Name the blood parasite species.
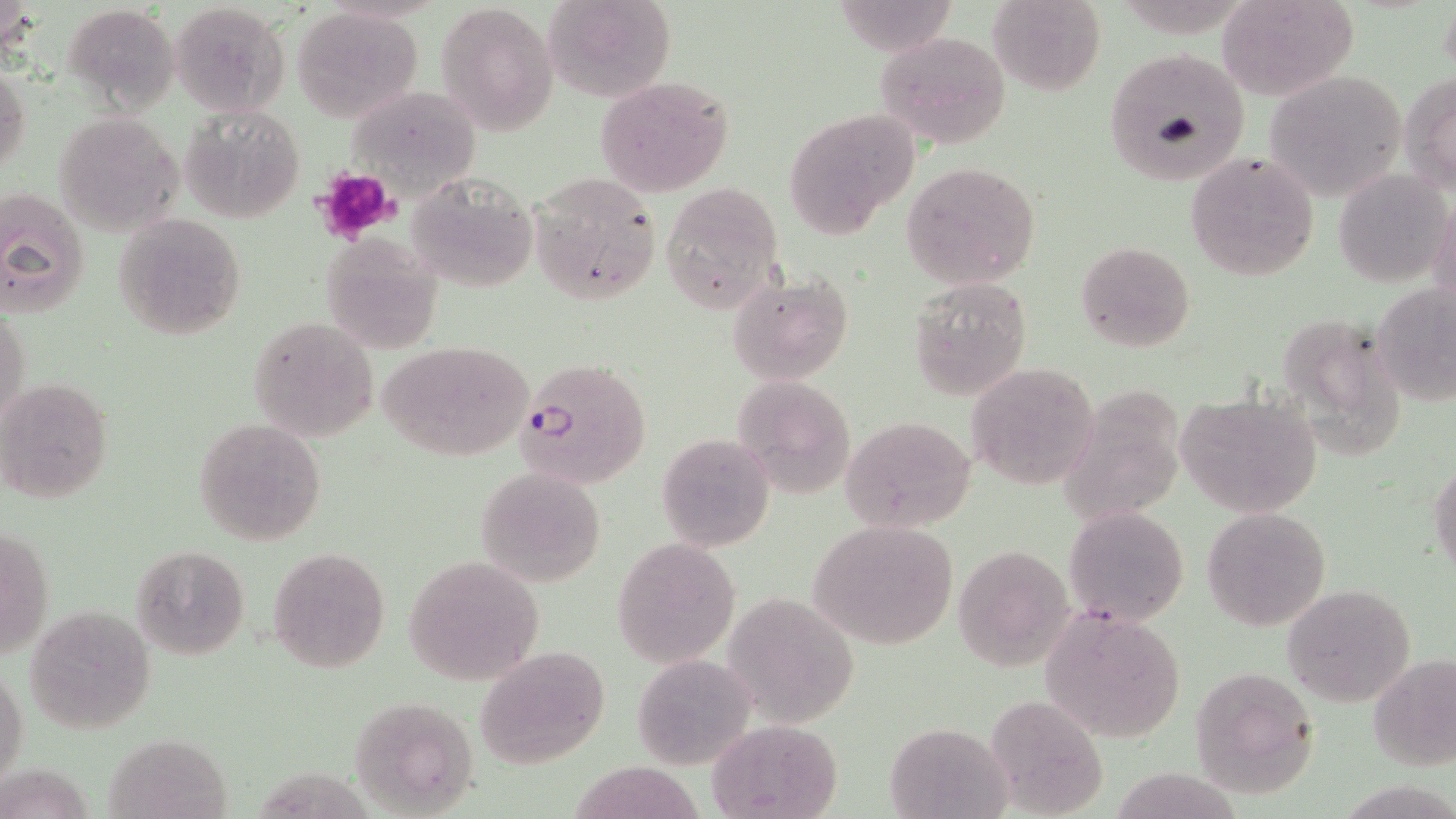

Plasmodium falciparum.

Approximate bounding boxes as (x1, y1, x2, y2) in pixels. Platelet locations: (314, 168, 399, 244). Plasmodium falciparum-infected red blood cell locations: (513, 358, 654, 489). Uninfected red blood cell locations: (544, 0, 676, 103), (842, 0, 960, 55), (989, 0, 1106, 95), (1218, 0, 1359, 101), (63, 1, 180, 109), (437, 2, 560, 135), (170, 3, 288, 115), (288, 7, 422, 121), (875, 31, 1012, 146), (1102, 48, 1251, 188), (0, 64, 30, 181), (1262, 69, 1407, 201), (1403, 69, 1456, 195), (593, 74, 735, 198), (180, 106, 305, 221), (783, 109, 918, 237), (55, 110, 182, 236), (1186, 152, 1319, 281), (902, 161, 1040, 289), (1334, 168, 1452, 288), (528, 171, 662, 305), (405, 174, 537, 292), (658, 183, 782, 315), (0, 186, 91, 317), (113, 214, 246, 339), (320, 234, 444, 353), (1076, 240, 1195, 351), (726, 270, 852, 385), (906, 276, 1034, 399), (1374, 284, 1455, 405), (1, 305, 31, 434), (249, 317, 378, 442), (1286, 322, 1401, 461), (381, 341, 534, 462), (966, 361, 1099, 491), (1, 376, 114, 505), (730, 376, 855, 497), (1060, 386, 1189, 527), (1175, 392, 1324, 519), (840, 416, 978, 534), (195, 418, 327, 545), (658, 434, 774, 551), (1430, 462, 1456, 578), (474, 467, 607, 586), (1065, 505, 1188, 627), (1200, 507, 1331, 629), (810, 518, 959, 651), (1, 522, 51, 664), (614, 536, 740, 668), (132, 546, 250, 661), (951, 546, 1072, 670), (268, 547, 392, 672), (403, 554, 545, 686), (1282, 584, 1416, 706), (723, 590, 862, 725), (24, 606, 155, 735), (1042, 606, 1189, 744), (474, 647, 610, 767), (631, 652, 757, 770), (1370, 653, 1456, 772), (1, 663, 28, 792), (1188, 665, 1321, 797), (349, 696, 480, 816), (982, 696, 1107, 817), (707, 719, 843, 818), (883, 720, 1015, 819), (104, 732, 235, 819), (574, 757, 713, 819). Single field of view. Image is 1456×819 pixels. Captured at 1000x magnification. May-Grünwald-Giemsa stain. Light microscopy. Thin blood film.